Locate every leukocyte (white blood cell).
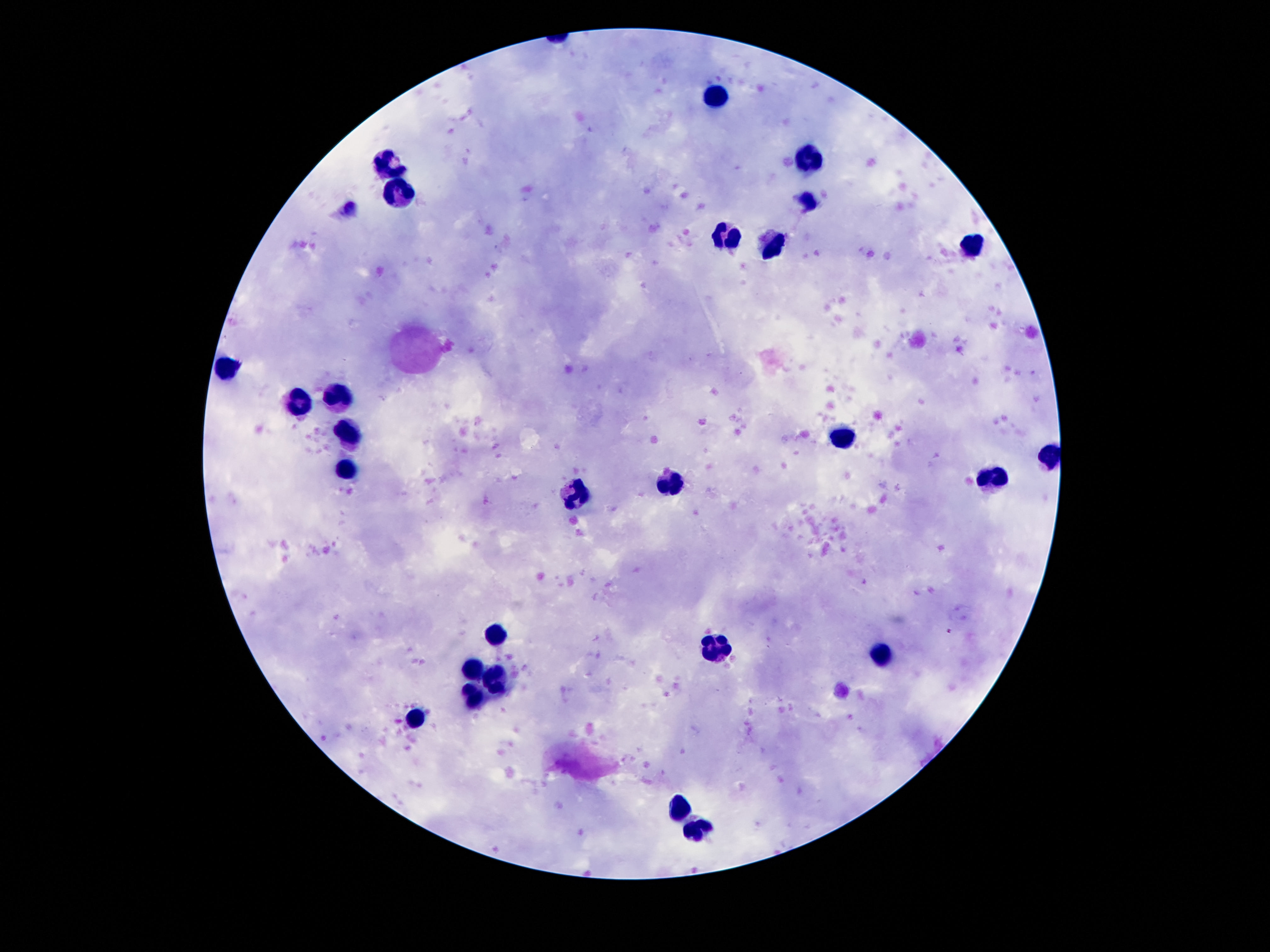
Approximate centers as {x, y} in pixels.
Leukocytes: {719, 95}, {808, 162}, {390, 163}, {397, 191}, {806, 198}, {726, 242}, {971, 243}, {774, 246}, {225, 366}, {342, 396}, {295, 400}, {350, 433}, {842, 440}, {1050, 454}, {349, 469}, {995, 480}, {666, 484}, {578, 493}, {496, 635}, {712, 645}, {880, 655}, {474, 667}, {496, 676}, {476, 694}, {416, 719}, {680, 808}, {700, 831}.

Patient malaria status: not infected. Single field of view. Thick peripheral-blood smear. Photographed through the microscope eyepiece with a smartphone camera. Giemsa-stained preparation. 100x magnification. Image is 1270×952 pixels.